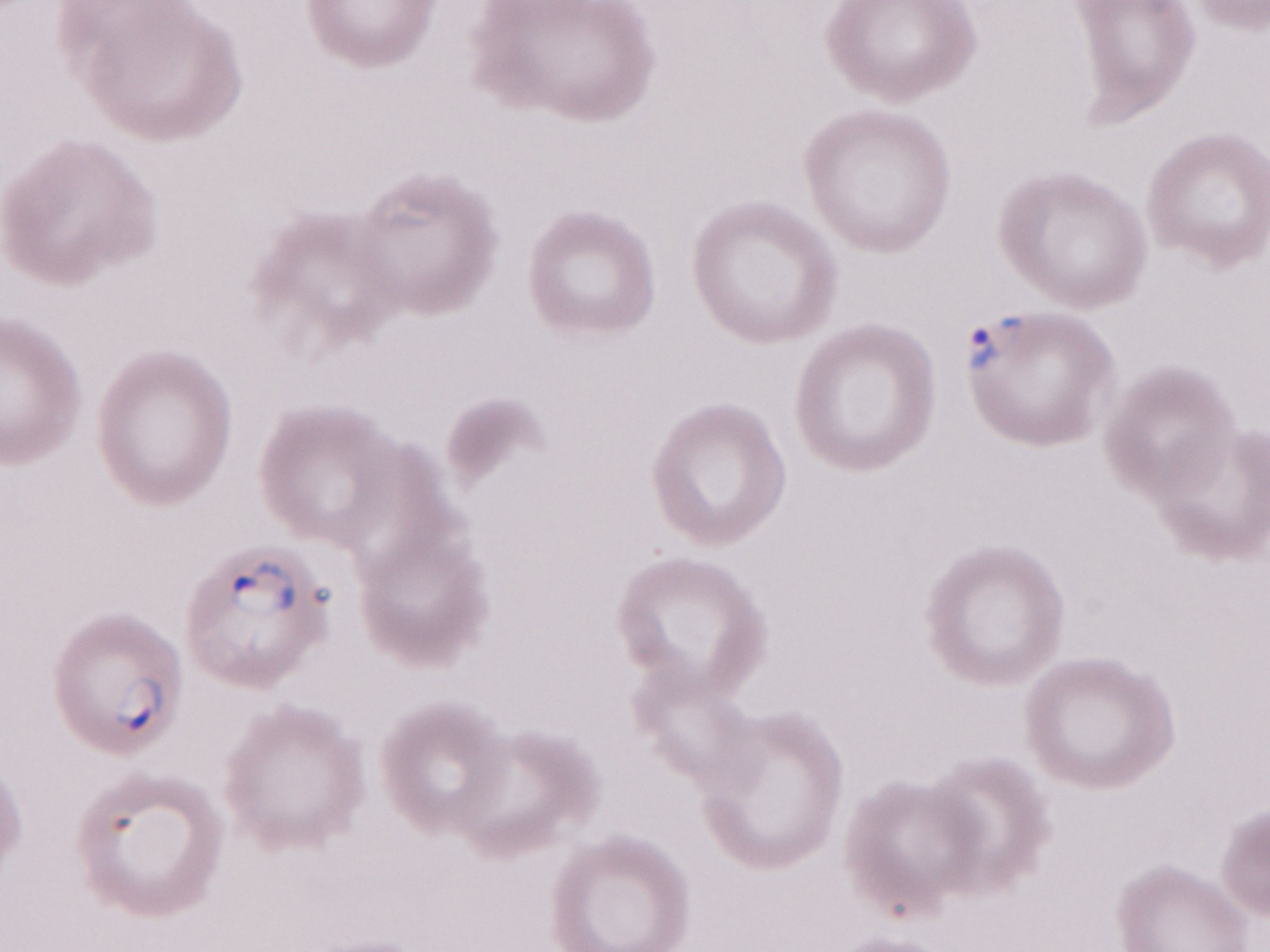 Magnification: 1,000x. One field of this slide. Patient-level malaria diagnosis: positive. Olympus BX43 microscope and DP73 digital camera. May-Grünwald-Giemsa (MGG) stain. Thin blood smear. Image is 1270×952 pixels.